Classify this cell by malaria status.
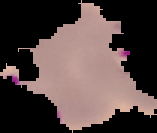
Parasitized.

preparation: thin blood smear
image_size: 157×133 pixels
image_type: segmented cell region with the area outside set to black